Assess this cell for malaria.
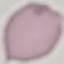
Uninfected.

Summary:
  - Stain: Giemsa
  - Preparation: thin smear
  - Image type: cell patch, automatically extracted from a larger field of view and resized to 64 × 64 pixels
  - Capture: smartphone through the microscope eyepiece